Describe the morphology of the erythrocytes.
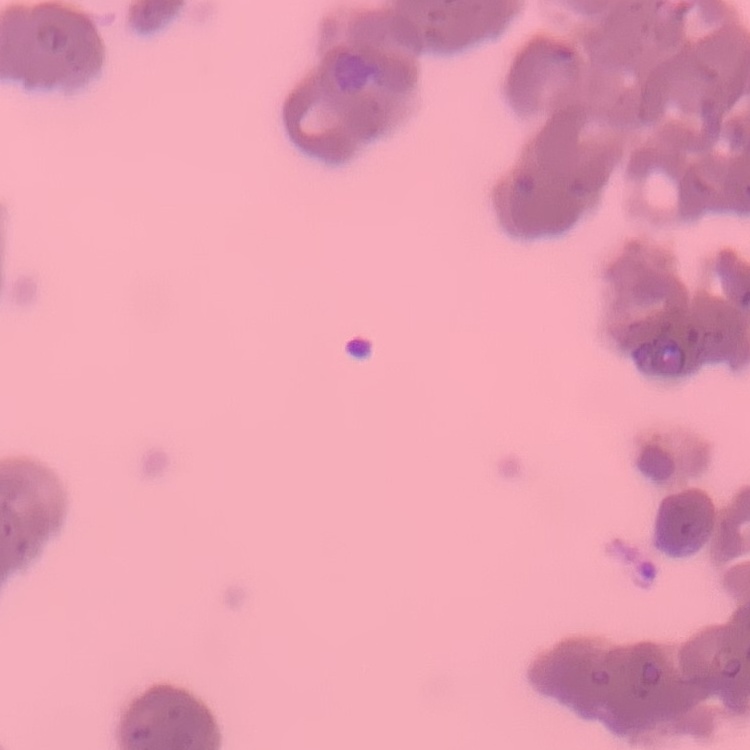
Rouleaux formation.

Summary:
  - Stain: Field's or Giemsa
  - Image type: square crop of a larger photomicrograph
  - Preparation: thin peripheral smear